Evaluate for malaria.
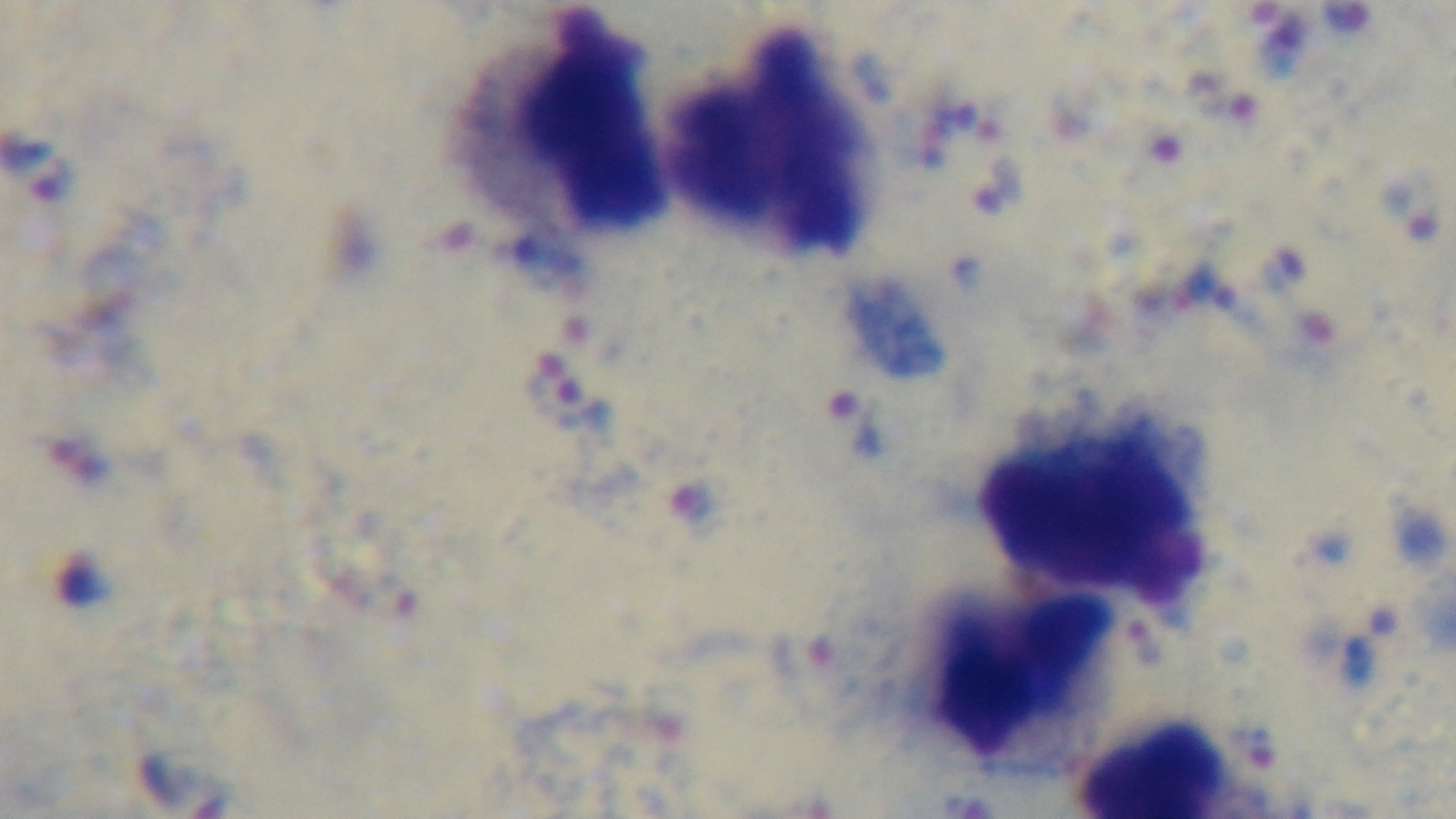
It is infected.

Summary:
  - Preparation: thick smear
  - Field of view: single
  - Stain: Giemsa
  - Objective: 100x oil immersion
  - Modality: light microscopy
  - Capture: mounted 4K digital camera